Locate every leukocyte (white blood cell).
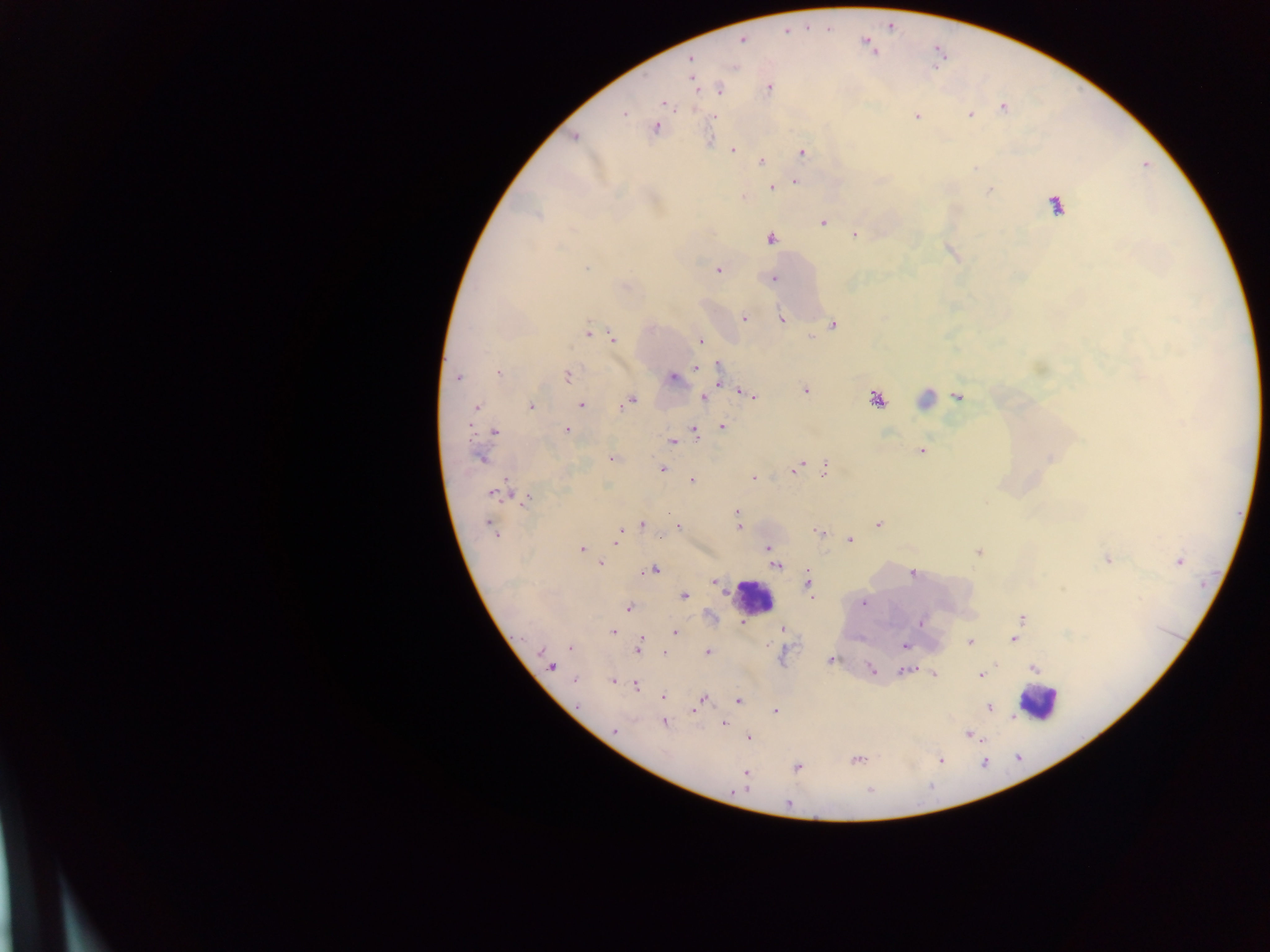

Approximate centers as [x, y] in pixels.
Leukocytes: [1055, 204], [754, 596], [1038, 702].

Summary:
  - Plasmodium parasite locations: [742, 39], [867, 43], [689, 59], [693, 81], [769, 87], [718, 89], [664, 103], [1002, 108], [623, 113], [970, 115], [712, 116], [916, 116], [655, 126], [573, 136], [733, 149], [801, 152], [799, 158], [762, 161], [794, 181], [776, 185], [772, 186], [989, 190], [743, 197], [822, 222], [853, 234], [770, 238], [587, 267], [718, 270], [773, 279], [744, 317], [782, 320], [833, 324], [587, 333], [810, 336], [611, 337], [700, 340], [718, 365], [695, 367], [498, 373], [566, 375], [456, 377], [671, 377], [718, 380], [804, 389], [743, 393], [751, 396], [703, 397], [958, 397], [876, 399], [925, 399], [628, 402], [530, 405], [581, 405], [476, 408], [722, 427], [567, 430], [694, 430], [493, 431], [672, 440], [921, 450], [479, 458], [612, 458], [1050, 458], [800, 466], [824, 468], [660, 469], [790, 470], [754, 478], [692, 480], [499, 492], [526, 497], [736, 512], [642, 524], [878, 524], [678, 527], [739, 527], [492, 528], [819, 533], [849, 539], [616, 541], [768, 548], [580, 549], [978, 552], [1107, 559], [1178, 561], [600, 563], [775, 565], [654, 569], [913, 573], [807, 581], [714, 582], [684, 596], [813, 598], [862, 602], [628, 607], [1022, 618], [920, 621], [742, 623], [740, 624], [781, 629], [612, 631], [675, 633], [1013, 639], [969, 641], [904, 646], [571, 647], [638, 647], [708, 652], [664, 653], [830, 660], [551, 666], [1033, 668], [871, 670], [904, 670], [934, 673], [980, 675], [574, 680], [613, 680], [635, 684], [663, 695], [702, 698], [738, 700], [987, 707], [773, 711], [1013, 716], [664, 722], [724, 723], [614, 731], [969, 735], [747, 737], [856, 759], [940, 760], [797, 767], [745, 773], [745, 782], [788, 804]
  - Field of view: single
  - Capture: mobile-phone photograph through a microscope
  - Image size: 1270×952 pixels
  - Country: Ghana
  - Preparation: thick blood smear